Locate leukocytes (white blood cells).
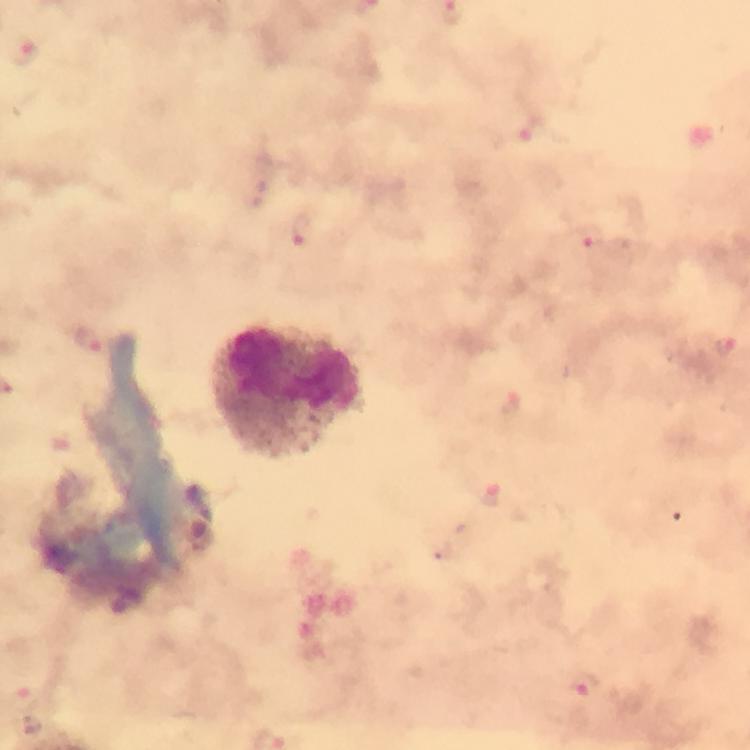
Approximate centers as {x, y} in pixels.
Leukocytes: {289, 393}.

Summary:
  - Malaria parasite locations: {25, 51}, {303, 231}, {591, 238}, {89, 342}, {727, 347}, {490, 499}, {586, 686}
  - Stain: Giemsa
  - Preparation: thick blood film
  - Cropped from: a single field of view
  - Capture: smartphone photograph through a microscope
  - Image size: 750×750 pixels
  - Context: from a malaria diagnostic workup
  - Magnification: 100x
  - Immersion oil: applied